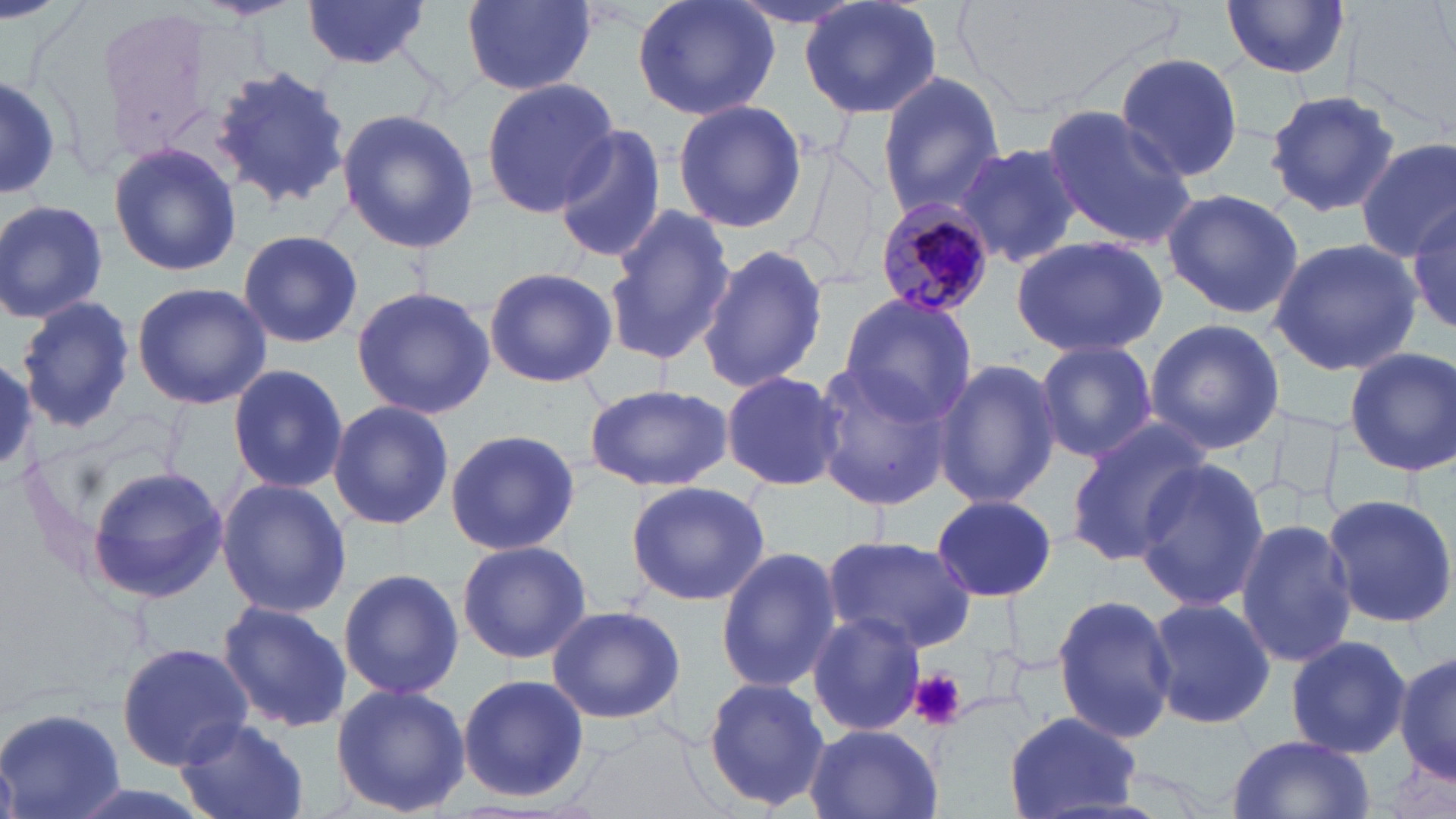
Approximate bounding boxes as named x1/y1/x2/y2 corners in pixels. Uninfected red blood cell locations: (x1=301, y1=0, x2=434, y2=69), (x1=462, y1=0, x2=596, y2=94), (x1=629, y1=0, x2=780, y2=123), (x1=723, y1=0, x2=877, y2=33), (x1=800, y1=0, x2=943, y2=121), (x1=1221, y1=0, x2=1352, y2=79), (x1=1114, y1=53, x2=1244, y2=182), (x1=210, y1=63, x2=353, y2=213), (x1=875, y1=71, x2=1006, y2=216), (x1=1, y1=72, x2=61, y2=202), (x1=480, y1=80, x2=619, y2=217), (x1=1267, y1=89, x2=1400, y2=219), (x1=671, y1=99, x2=808, y2=232), (x1=1039, y1=103, x2=1200, y2=249), (x1=336, y1=110, x2=480, y2=253), (x1=552, y1=124, x2=666, y2=266), (x1=108, y1=139, x2=244, y2=277), (x1=1354, y1=139, x2=1456, y2=261), (x1=790, y1=141, x2=884, y2=291), (x1=956, y1=141, x2=1084, y2=269), (x1=1160, y1=188, x2=1304, y2=320), (x1=0, y1=199, x2=109, y2=323), (x1=1410, y1=204, x2=1456, y2=337), (x1=603, y1=205, x2=734, y2=368), (x1=236, y1=229, x2=363, y2=350), (x1=1010, y1=234, x2=1169, y2=359), (x1=1269, y1=236, x2=1424, y2=375), (x1=698, y1=240, x2=829, y2=394), (x1=483, y1=266, x2=619, y2=387), (x1=131, y1=281, x2=271, y2=410), (x1=351, y1=286, x2=496, y2=419), (x1=836, y1=292, x2=977, y2=426), (x1=17, y1=295, x2=137, y2=434), (x1=1144, y1=317, x2=1284, y2=455), (x1=1033, y1=340, x2=1159, y2=463), (x1=1344, y1=347, x2=1455, y2=476), (x1=0, y1=356, x2=38, y2=477), (x1=933, y1=358, x2=1061, y2=510), (x1=807, y1=361, x2=958, y2=510), (x1=227, y1=363, x2=348, y2=495), (x1=721, y1=370, x2=845, y2=493), (x1=583, y1=382, x2=732, y2=492), (x1=327, y1=399, x2=454, y2=531), (x1=1063, y1=421, x2=1214, y2=564), (x1=445, y1=426, x2=582, y2=556), (x1=1134, y1=459, x2=1270, y2=612), (x1=86, y1=464, x2=227, y2=603), (x1=216, y1=478, x2=352, y2=618), (x1=624, y1=481, x2=771, y2=605), (x1=1319, y1=493, x2=1456, y2=628), (x1=931, y1=494, x2=1056, y2=600), (x1=1236, y1=518, x2=1358, y2=669), (x1=820, y1=535, x2=977, y2=653), (x1=456, y1=539, x2=592, y2=666), (x1=715, y1=548, x2=843, y2=694), (x1=337, y1=567, x2=464, y2=699), (x1=1051, y1=593, x2=1178, y2=743), (x1=1143, y1=596, x2=1277, y2=728), (x1=217, y1=599, x2=351, y2=733), (x1=543, y1=606, x2=687, y2=723), (x1=806, y1=611, x2=924, y2=738), (x1=1283, y1=634, x2=1410, y2=760), (x1=117, y1=641, x2=256, y2=769), (x1=1393, y1=644, x2=1454, y2=791), (x1=457, y1=673, x2=589, y2=804), (x1=701, y1=676, x2=831, y2=812), (x1=331, y1=682, x2=471, y2=817), (x1=0, y1=706, x2=124, y2=819), (x1=1005, y1=711, x2=1140, y2=818), (x1=177, y1=716, x2=308, y2=819), (x1=803, y1=724, x2=945, y2=819), (x1=1225, y1=734, x2=1375, y2=819). Platelet locations: (x1=909, y1=668, x2=967, y2=731). Plasmodium malariae-infected red blood cell locations: (x1=873, y1=198, x2=995, y2=317). Slide-level diagnosis: Plasmodium malariae. Captured at 1000x magnification. Thin blood film. Optical microscopy. One field of a larger specimen. Image is 1456×819 pixels. May-Grünwald-Giemsa stain.